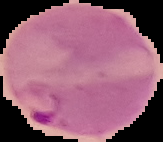
{
  "result": "Plasmodium parasites identified",
  "image_size": "163×142 pixels",
  "image_type": "cell region segmented out of the field of view; surrounding area masked to black",
  "preparation": "thin blood smear"
}